Comment on the morphology of the red blood cells.
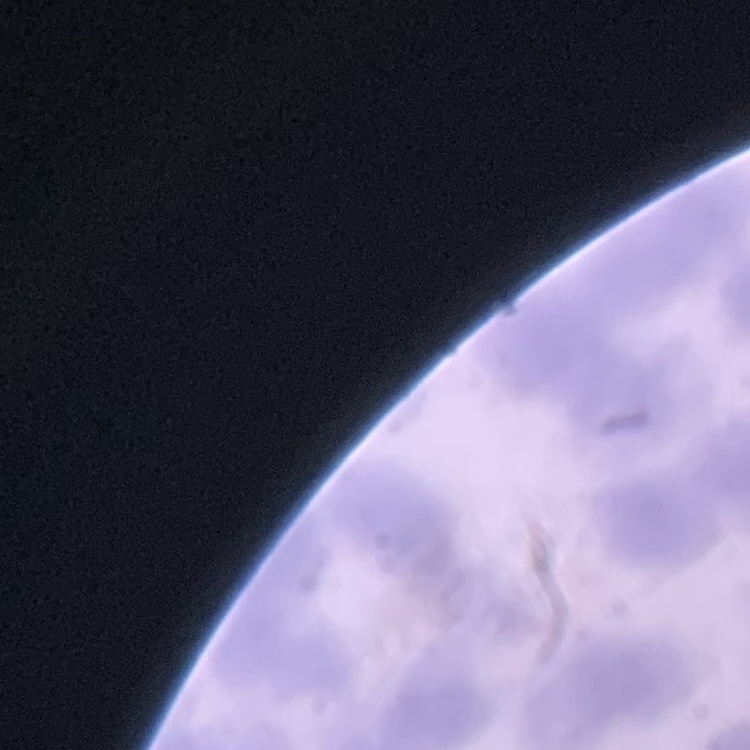
They show rouleaux formation.

One tile cut from a larger photomicrograph. Thin peripheral smear. Stained with either Field's or Giemsa.